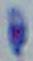

identification: Toxoplasma gondii
modality: micrograph
magnification: 1000x